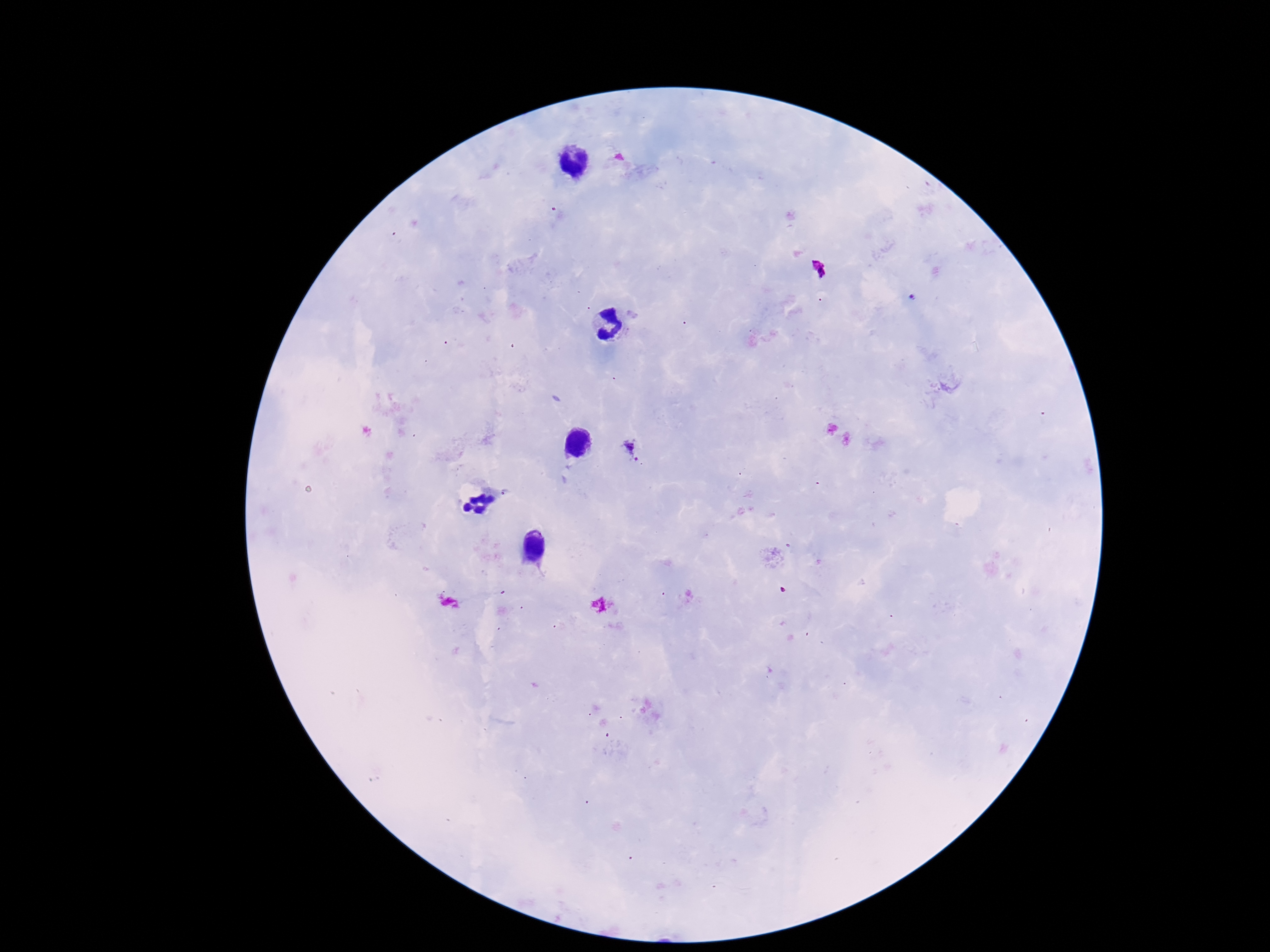 Approximate centers as {x, y} in pixels. Plasmodium parasite locations: {913, 298}, {630, 450}. Giemsa-stained preparation. Image is 1270×952 pixels. Thick blood film. Smartphone photograph taken through the microscope eyepiece. 100x magnification. Patient malaria status: positive. One field from this slide.